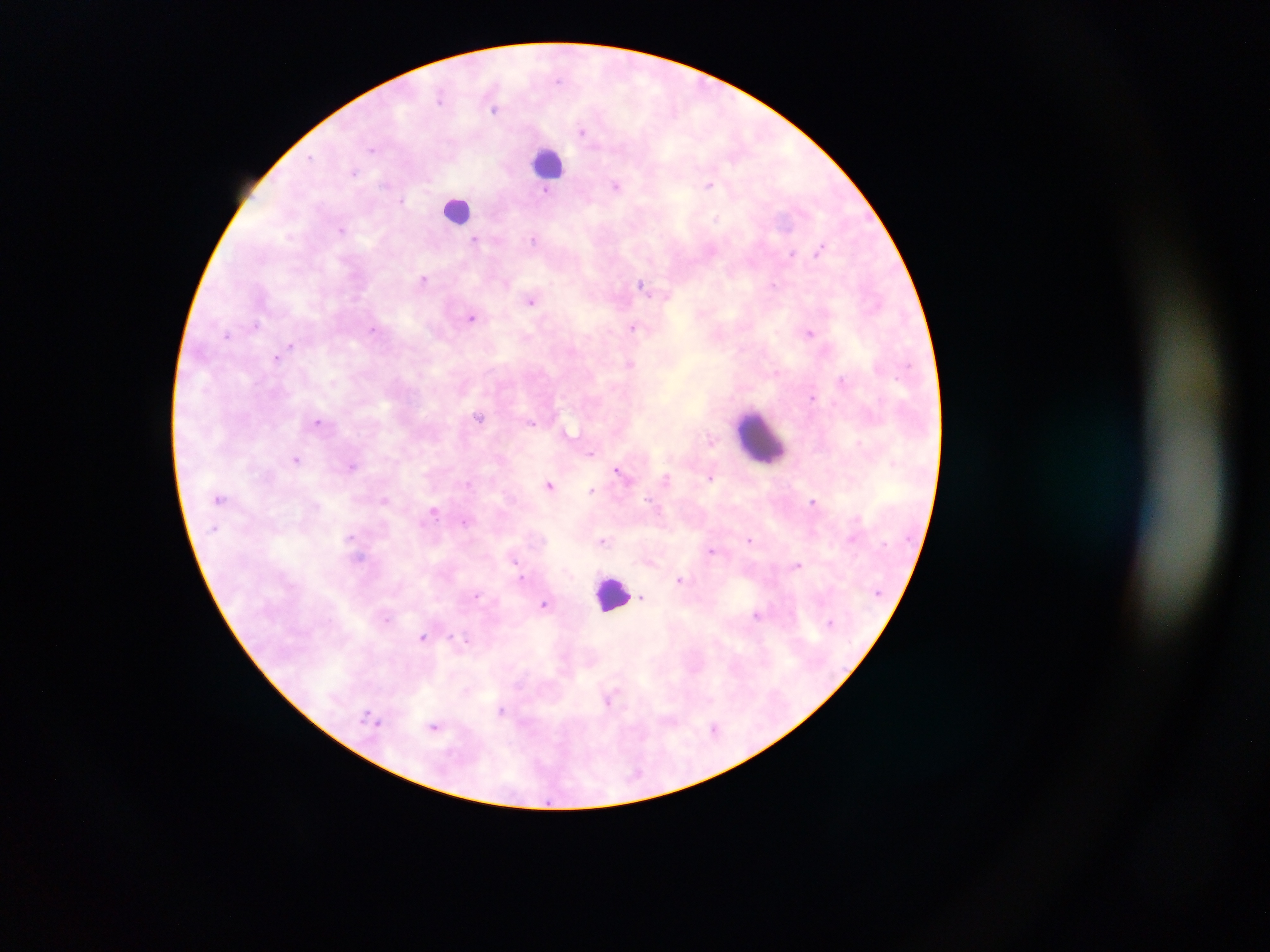 Approximate centers as [x, y] in pixels. Malaria parasite locations: [559, 81], [440, 96], [495, 109], [582, 131], [372, 149], [311, 158], [355, 172], [709, 184], [616, 186], [546, 191], [402, 200], [716, 218], [341, 229], [534, 239], [474, 240], [820, 249], [792, 253], [424, 279], [507, 284], [641, 284], [773, 284], [531, 301], [471, 318], [256, 325], [632, 327], [374, 330], [810, 332], [227, 335], [291, 345], [276, 358], [630, 364], [841, 379], [812, 397], [479, 417], [317, 421], [533, 423], [710, 440], [859, 442], [591, 453], [296, 459], [352, 465], [617, 471], [666, 478], [710, 478], [468, 483], [550, 484], [592, 490], [648, 499], [384, 500], [813, 501], [434, 512], [857, 517], [464, 521], [351, 537], [852, 538], [750, 540], [603, 541], [712, 551], [359, 558], [514, 559], [798, 565], [522, 578], [680, 579], [478, 595], [643, 598], [544, 604], [757, 614], [387, 619], [422, 637], [451, 637], [466, 640], [610, 699], [501, 711], [367, 712], [378, 723], [434, 726], [714, 728]. Leukocyte locations: [549, 162], [457, 209], [761, 438], [611, 593]. Sample from Ghana. Image is 1270×952 pixels. Single field of view. Photographed through a microscope with a mobile-phone camera. Thick blood film.